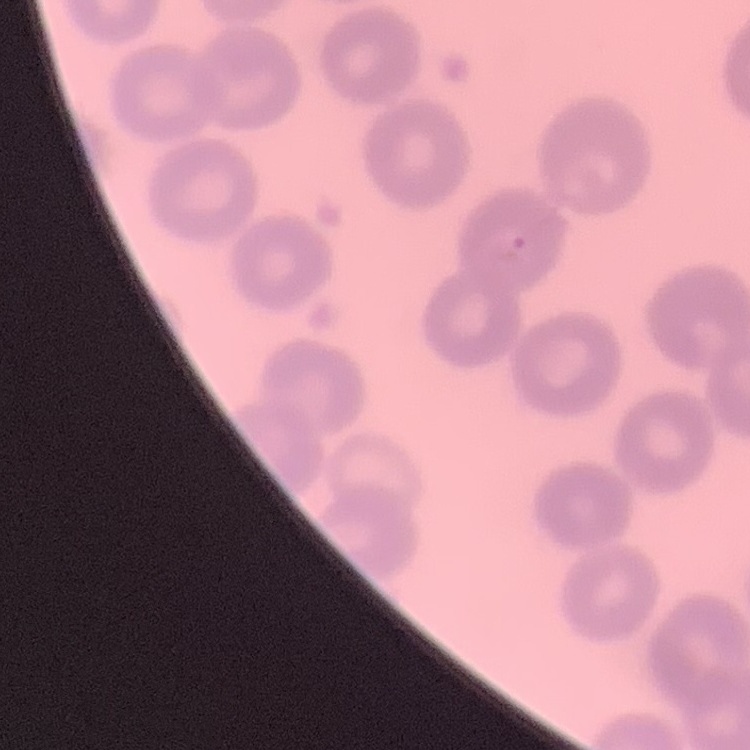 The red blood cells show no rouleaux formation. One tile cut from a larger photomicrograph. Thin peripheral smear. Stained with either Field's or Giemsa.